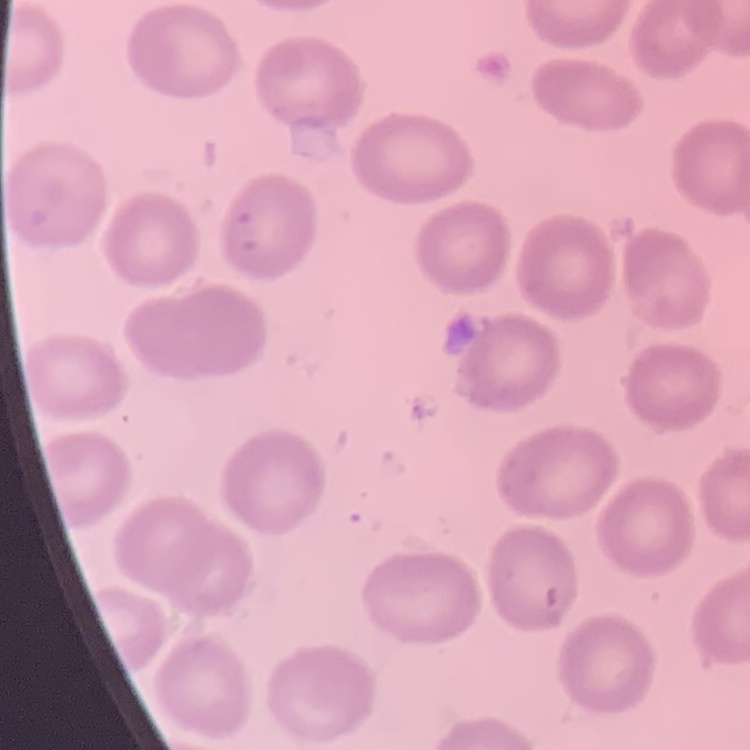

The red blood cells exhibit no rouleaux formation. Square crop of a larger photomicrograph. Thin blood film. Field's or Giemsa stain.